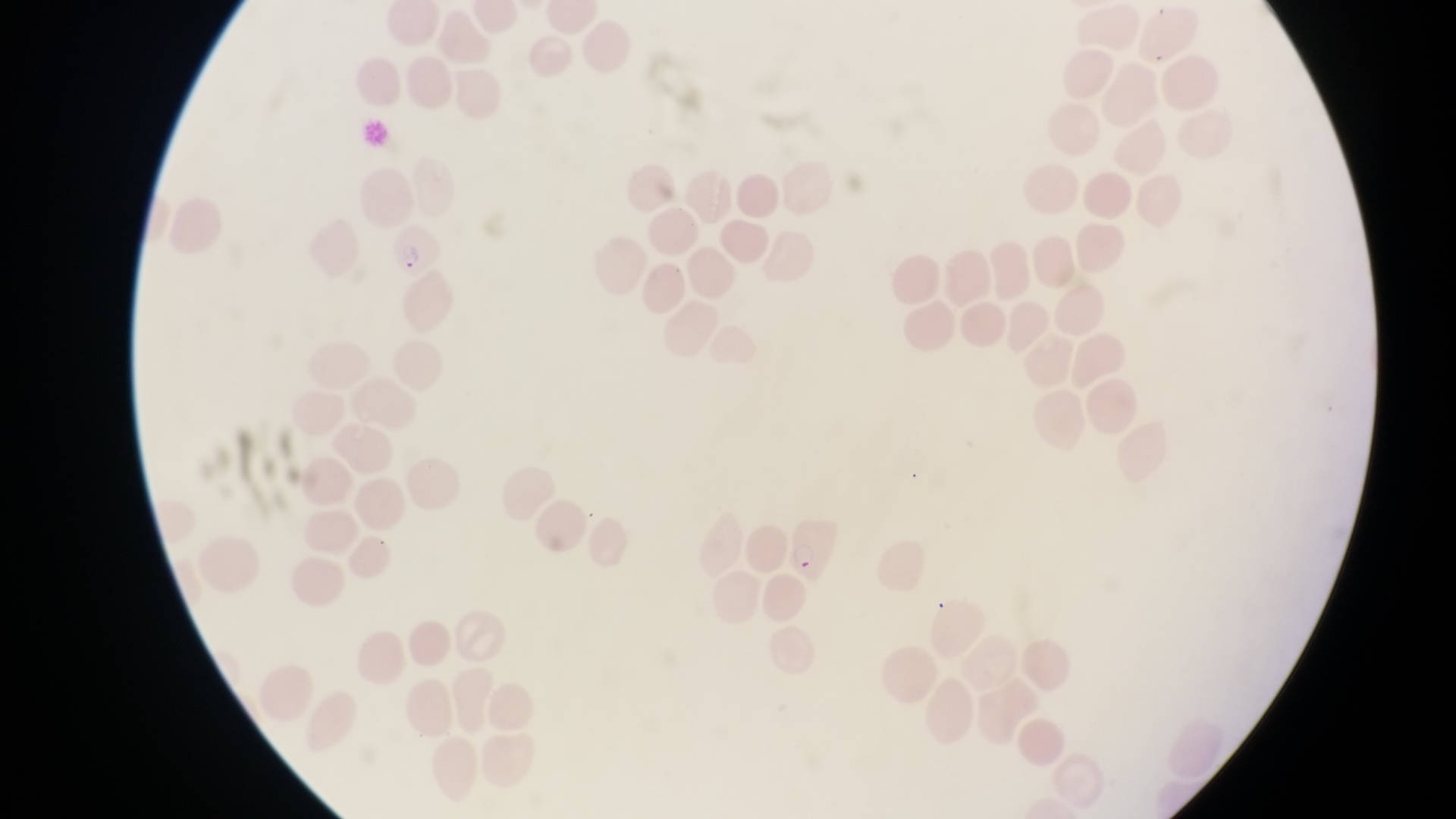
magnification = 1000x
capture = smartphone photograph through the eyepiece of an Olympus CX-23 microscope
country = Uganda
image size = 1456×819 pixels
field of view = single
parasitised red blood cell locations = approximate bounding boxes as {left, top, right, bottom} in pixels: {384, 224, 440, 284}, {786, 518, 841, 582}
preparation = thin blood film